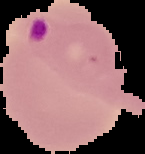
preparation = thin blood smear
result = Plasmodium parasites detected
image size = 145×154 pixels
image type = segmented cell region with the area outside set to black